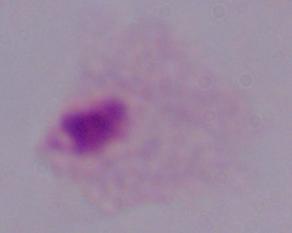
Summary:
  - Modality: micrograph
  - Magnification: 1000x
  - Identification: trichomonad